Assess this cell for malaria.
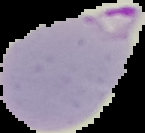
It is parasitized.

Summary:
  - Image size: 145×133 pixels
  - Preparation: thin blood film
  - Image type: segmented cell region on a black background